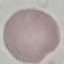 Result: no malaria parasites detected. Thin blood film. Giemsa stain. Photographed with a smartphone camera at the microscope eyepiece. Cell patch, automatically extracted from a larger field of view and resized to 64 × 64 pixels.